Name the parasite shown.
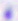
Toxoplasma gondii.

{
  "magnification": "400x",
  "modality": "micrograph"
}